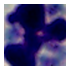
1000x magnification. A white blood cell is seen. Micrograph.